Report the malaria status of this cell.
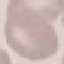
Uninfected.

Automatically extracted cell patch, resized to 64 × 64 pixels. Thin blood film. Giemsa-stained preparation. Acquired by smartphone through the microscope eyepiece.